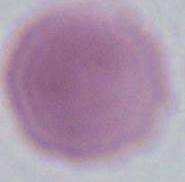
An erythrocyte is shown. Photomicrograph. Captured at 1000x magnification.